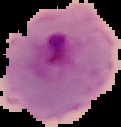

Summary:
  - Preparation: thin blood smear
  - Image size: 121×127 pixels
  - Image type: segmented cell region with the area outside set to black
  - Malaria status: parasitized